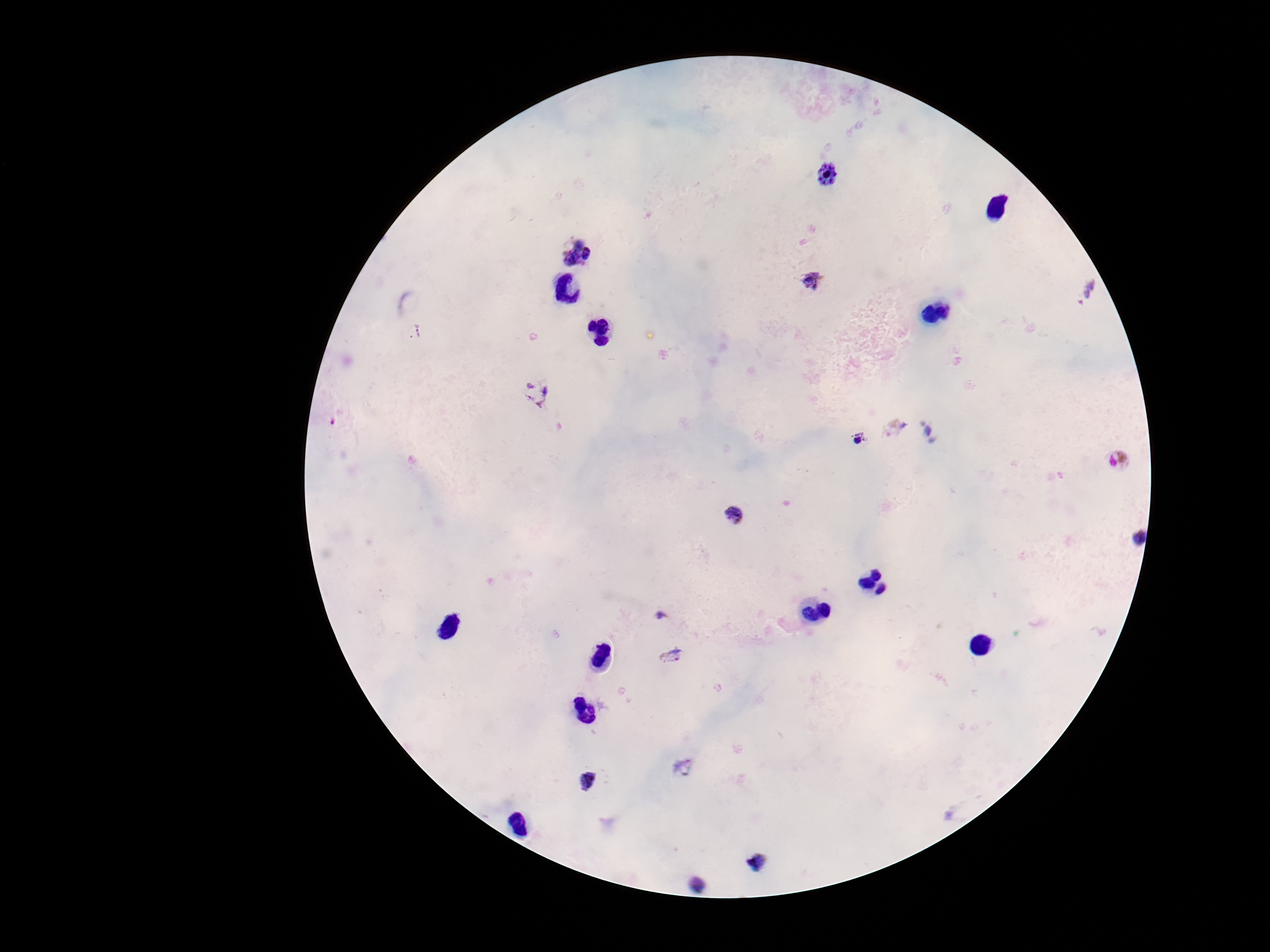
preparation = thick blood smear
image size = 1270×952 pixels
stain = Giemsa
field of view = one from this slide
capture = smartphone camera through the microscope eyepiece
patient malaria status = infected
Plasmodium parasite locations = approximate object centers, in pixels from the top-left corner: (x=827, y=176), (x=578, y=254), (x=815, y=281), (x=1084, y=291), (x=415, y=332), (x=537, y=393), (x=332, y=421), (x=894, y=427), (x=931, y=431), (x=860, y=439), (x=1119, y=461), (x=736, y=517), (x=1134, y=536), (x=661, y=617), (x=671, y=655), (x=682, y=766), (x=589, y=780), (x=756, y=861), (x=698, y=883)
magnification = 100x